Describe the morphology of the red blood cells.
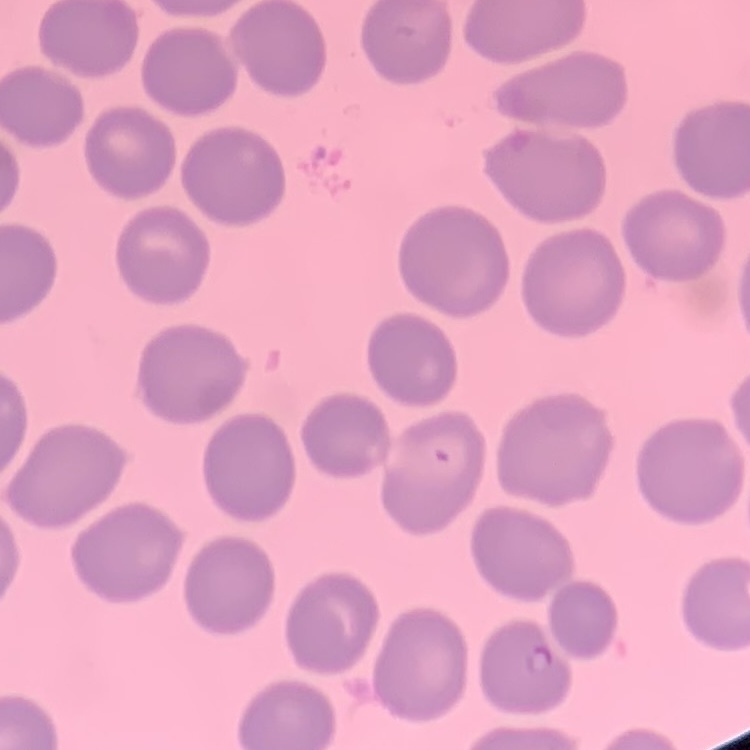
They show no rouleaux formation.

stain = Field's or Giemsa
preparation = thin blood film
image type = square crop of a larger photomicrograph